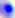
Summary:
  - Modality: micrograph
  - Magnification: 400x
  - Identification: Toxoplasma gondii